Classify this cell by malaria status.
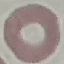
Uninfected.

Summary:
  - Image type: automatically extracted cell patch, resized to 64 × 64 pixels
  - Stain: Giemsa
  - Preparation: thin smear
  - Capture: smartphone through the microscope eyepiece